Look for Plasmodium parasites.
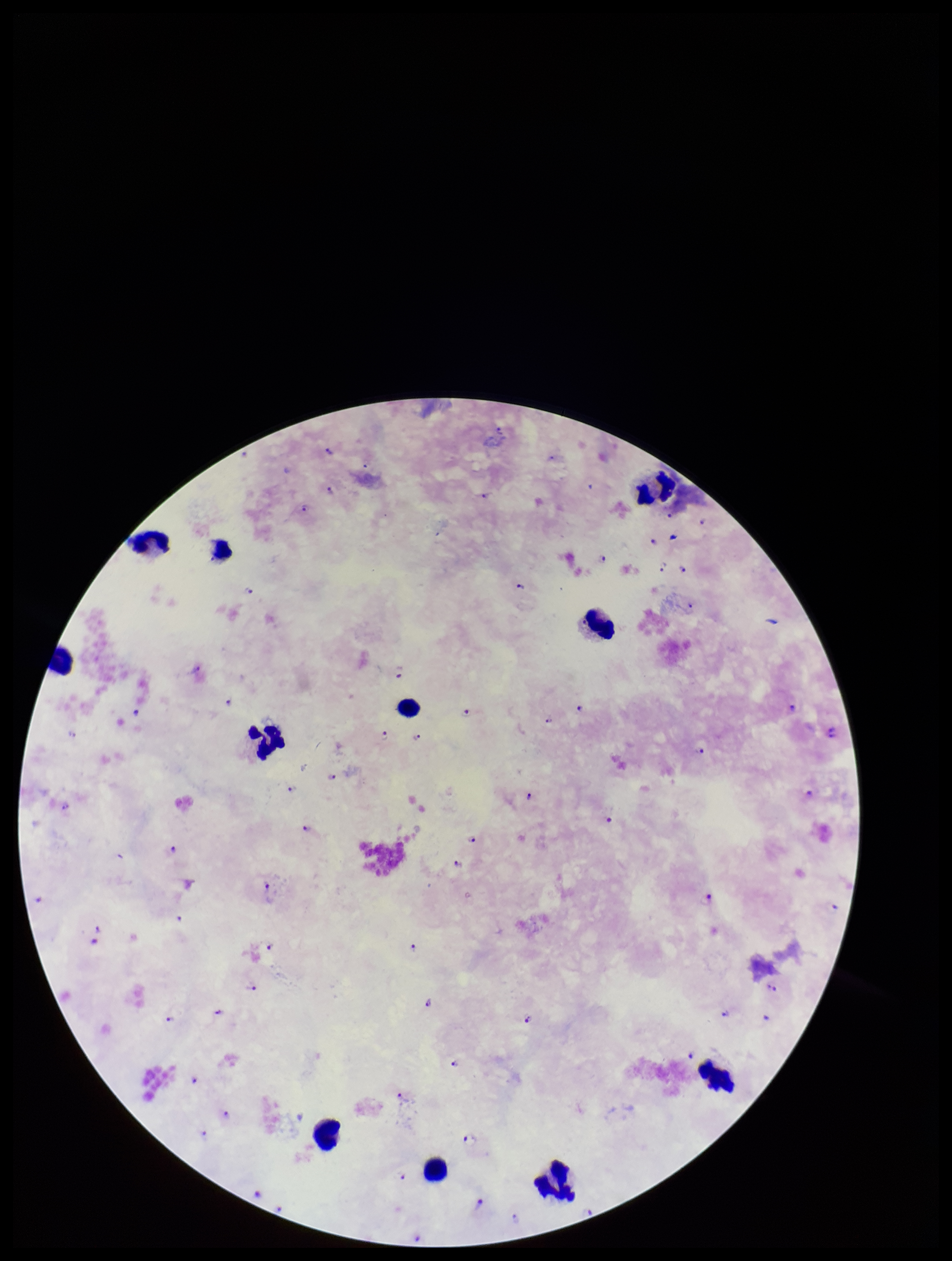
Seen.

Summary:
  - Parasite count: 52
  - Leukocyte count: 11
  - Preparation: thick blood smear
  - Field of view: single
  - Image size: 952×1261 pixels
  - Stain: Giemsa
  - Capture: smartphone photograph through the microscope eyepiece
  - Species reported for this patient: Plasmodium falciparum
  - Patient malaria status: infected